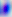
Summary:
  - Magnification: 400x
  - Identification: Toxoplasma gondii
  - Modality: micrograph